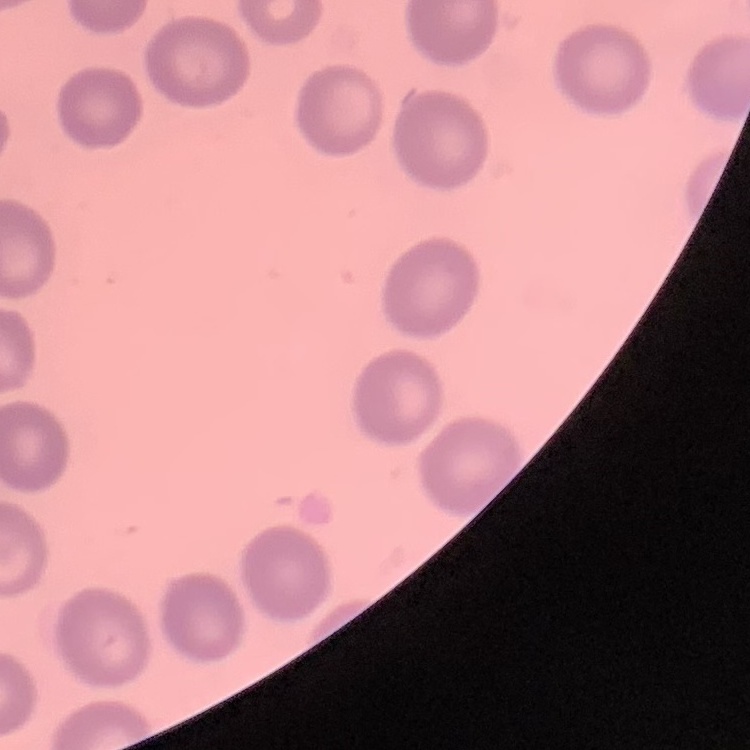
red blood cell morphology = no rouleaux formation
preparation = thin blood smear
stain = Field's or Giemsa
image type = square crop of a larger photomicrograph